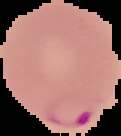
Summary:
  - Image size: 121×136 pixels
  - Preparation: thin blood film
  - Result: Plasmodium parasites detected
  - Image type: segmented cell region with the area outside set to black